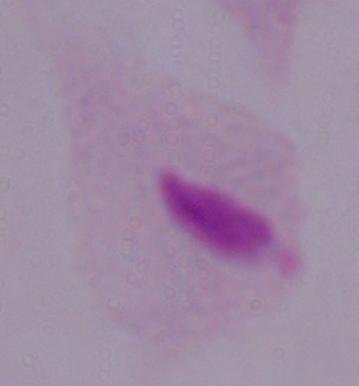

Captured at 1000x magnification. A trichomonad is seen. Photomicrograph.